Evaluate for Plasmodium parasites.
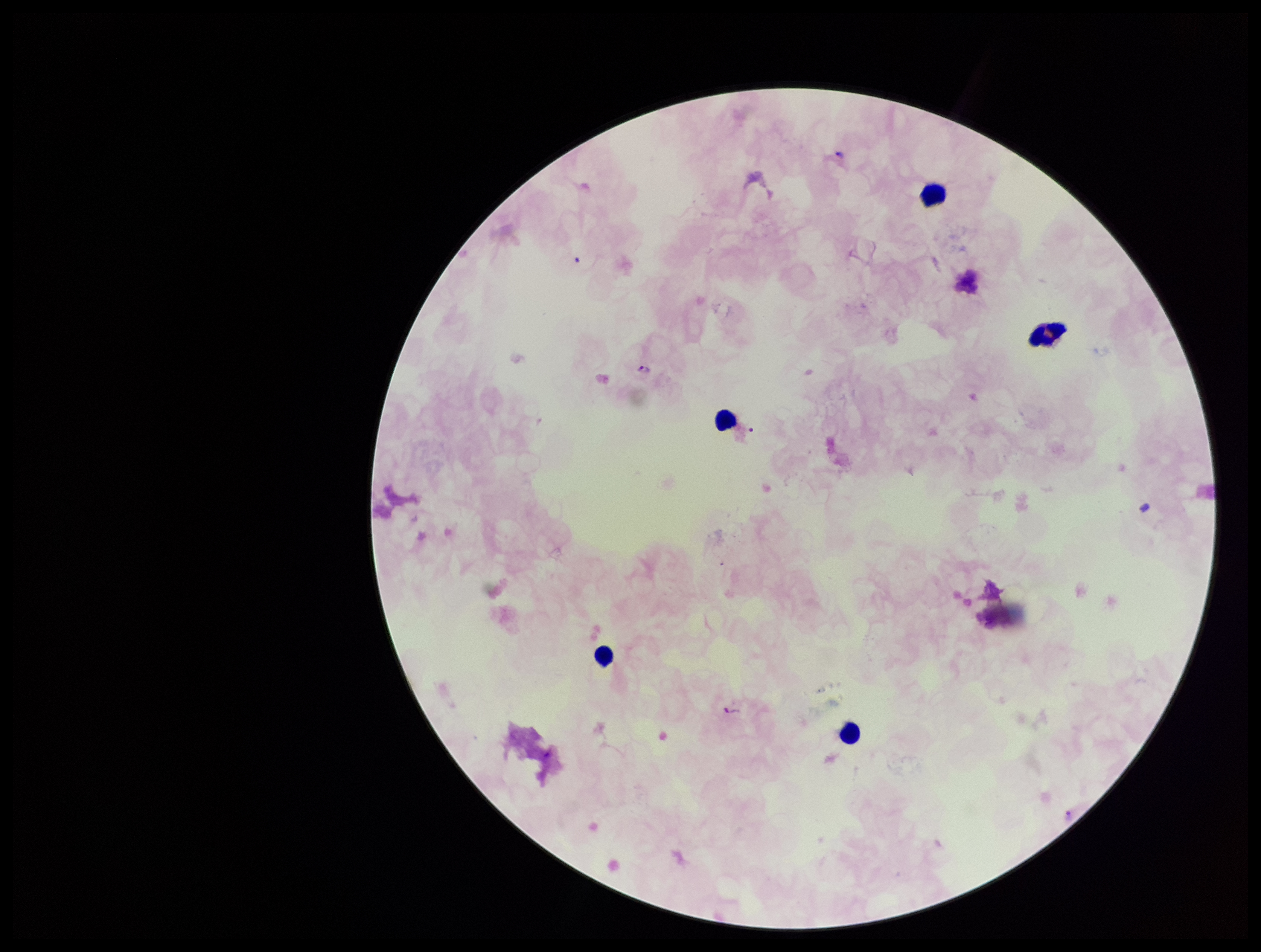
Detected.

Summary:
  - Leukocyte count: 5
  - Species reported for this patient: Plasmodium falciparum
  - Patient malaria status: infected
  - Capture: smartphone photograph through the microscope eyepiece
  - Parasite count: 2
  - Stain: Giemsa
  - Image size: 1261×952 pixels
  - Field of view: single
  - Preparation: thick blood smear